Comment on the morphology of the erythrocytes.
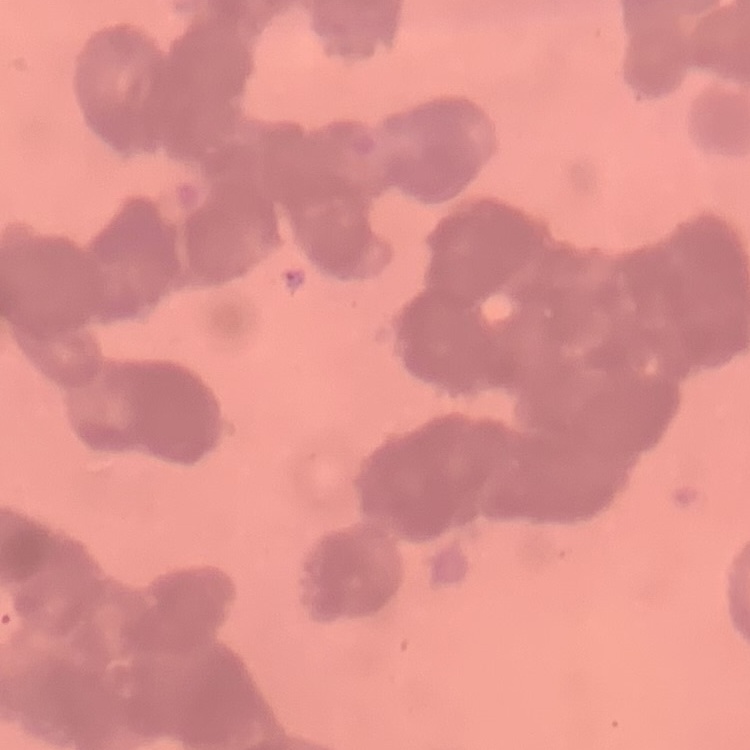
They show rouleaux formation.

{
  "image_type": "one tile cut from a larger photomicrograph",
  "stain": "Field's or Giemsa",
  "preparation": "thin blood smear"
}